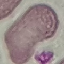
Result: negative for malaria parasites. Acquired by smartphone through the microscope eyepiece. Thin blood film. Cell patch, automatically extracted from a larger field of view and resized to 64 × 64 pixels. Giemsa-stained preparation.